Report the malaria status of this cell.
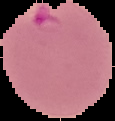

Parasitized.

Summary:
  - Image type: segmented cell region on a black background
  - Preparation: thin blood smear
  - Image size: 115×121 pixels